Comment on the morphology of the erythrocytes.
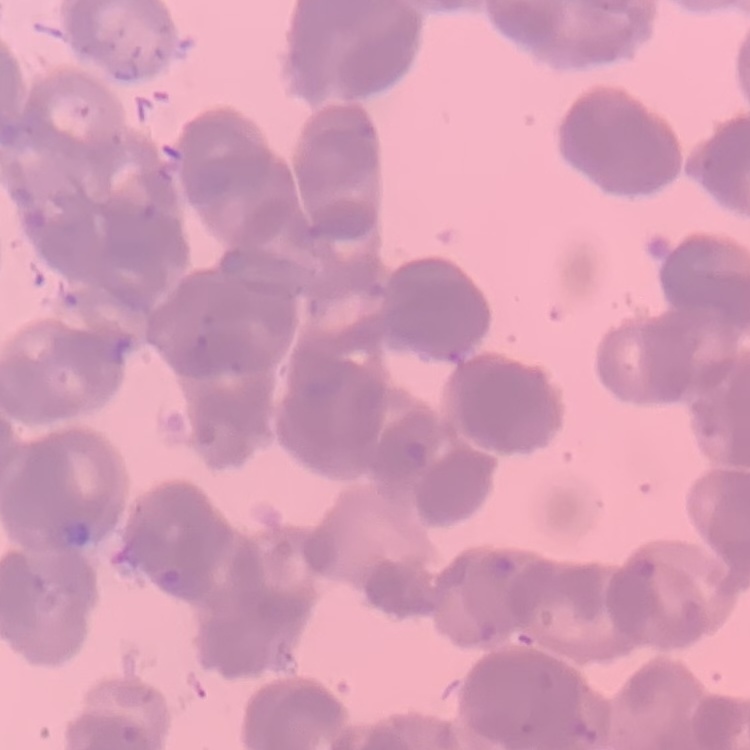

They show rouleaux formation.

Summary:
  - Preparation: thin peripheral smear
  - Image type: square crop of a larger photomicrograph
  - Stain: Field's or Giemsa